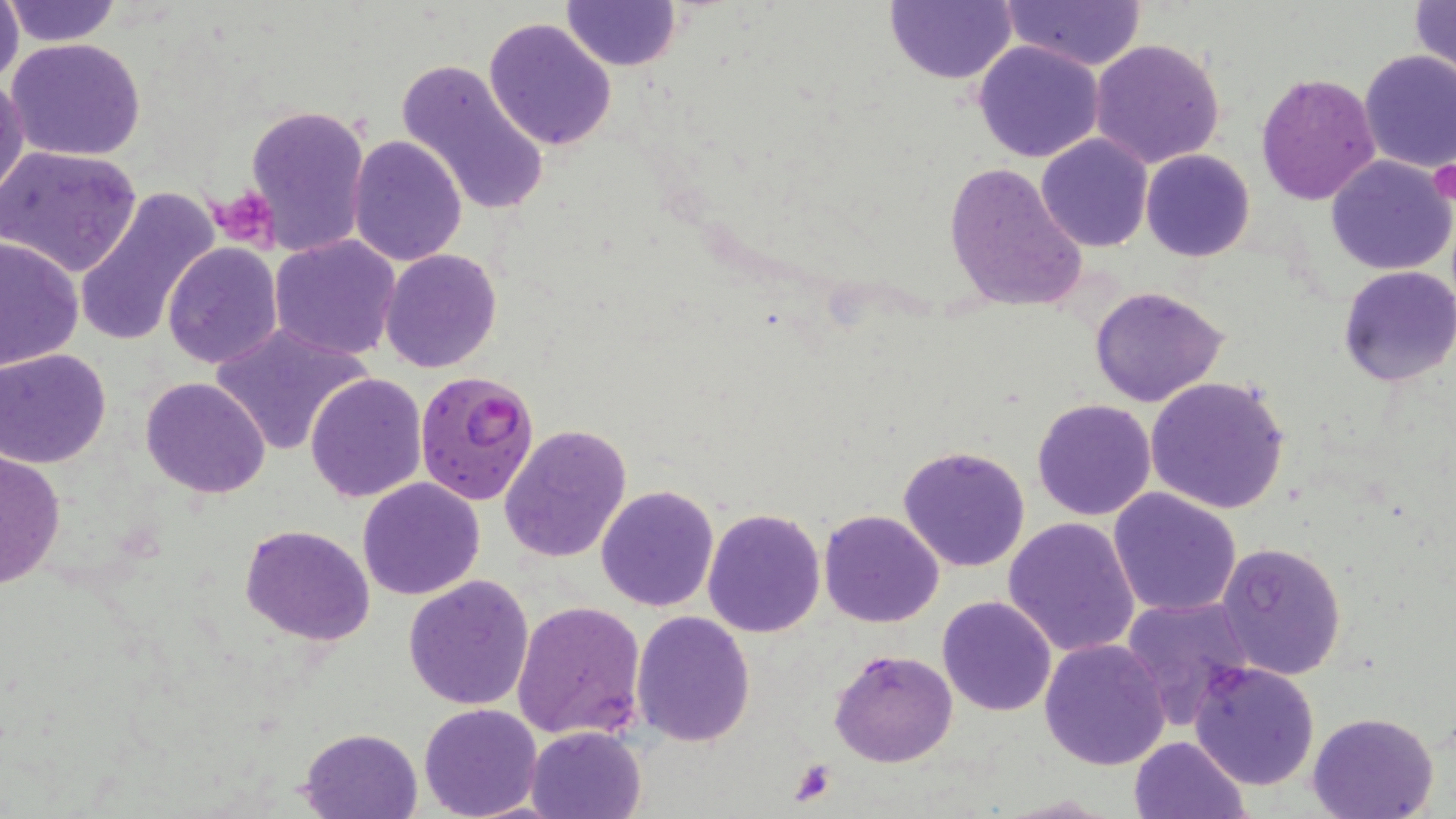

{
  "slide_level_diagnosis": "Plasmodium falciparum",
  "magnification": "1000x",
  "field_of_view": "single",
  "platelet_locations": "approximate bounding boxes as (x1, y1, x2, y2) in pixels: (1429, 154, 1456, 211), (213, 184, 280, 249), (788, 759, 838, 807)",
  "image_size": "1456×819 pixels",
  "preparation": "thin blood smear",
  "stain": "May-Grünwald-Giemsa",
  "uninfected_red_blood_cell_locations": "approximate bounding boxes as (x1, y1, x2, y2) in pixels: (0, 0, 24, 90), (561, 0, 681, 71), (886, 0, 1018, 85), (1409, 0, 1455, 88), (1, 1, 122, 49), (1002, 1, 1150, 72), (481, 17, 617, 154), (6, 37, 147, 162), (1089, 39, 1227, 169), (973, 40, 1105, 163), (1358, 51, 1456, 173), (396, 56, 550, 219), (0, 73, 26, 201), (1254, 73, 1381, 206), (245, 102, 370, 259), (347, 134, 468, 266), (1037, 134, 1153, 253), (0, 145, 142, 277), (1141, 149, 1255, 262), (1326, 156, 1455, 277), (941, 161, 1088, 311), (74, 186, 220, 347), (0, 235, 84, 371), (270, 235, 402, 359), (163, 242, 283, 368), (379, 248, 503, 373), (1337, 266, 1455, 387), (1089, 286, 1231, 408), (209, 323, 371, 456), (0, 349, 111, 467), (305, 372, 427, 504), (141, 375, 270, 498), (1145, 376, 1289, 514), (1031, 398, 1158, 521), (500, 422, 633, 563), (899, 443, 1032, 573), (0, 448, 65, 590), (357, 477, 485, 601), (596, 484, 721, 612), (1109, 488, 1242, 616), (702, 508, 827, 637), (819, 509, 945, 627), (1003, 517, 1142, 657), (240, 524, 376, 646), (1216, 540, 1347, 680), (402, 574, 534, 710), (938, 595, 1056, 716), (1121, 596, 1257, 726), (511, 600, 647, 743), (631, 610, 757, 745), (1039, 638, 1171, 772), (829, 648, 957, 768), (1188, 660, 1320, 791), (419, 703, 543, 818), (1307, 712, 1440, 819), (525, 725, 646, 819), (298, 728, 423, 819), (1128, 735, 1250, 818)",
  "modality": "light microscopy",
  "plasmodium_falciparum_infected_red_blood_cell_locations": "approximate bounding boxes as (x1, y1, x2, y2) in pixels: (415, 370, 542, 505)"
}